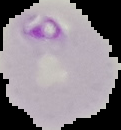 Segmented cell region on a black background. From a thin blood film. Result: Plasmodium parasites detected. Image is 121×130 pixels.